Locate every malaria parasite.
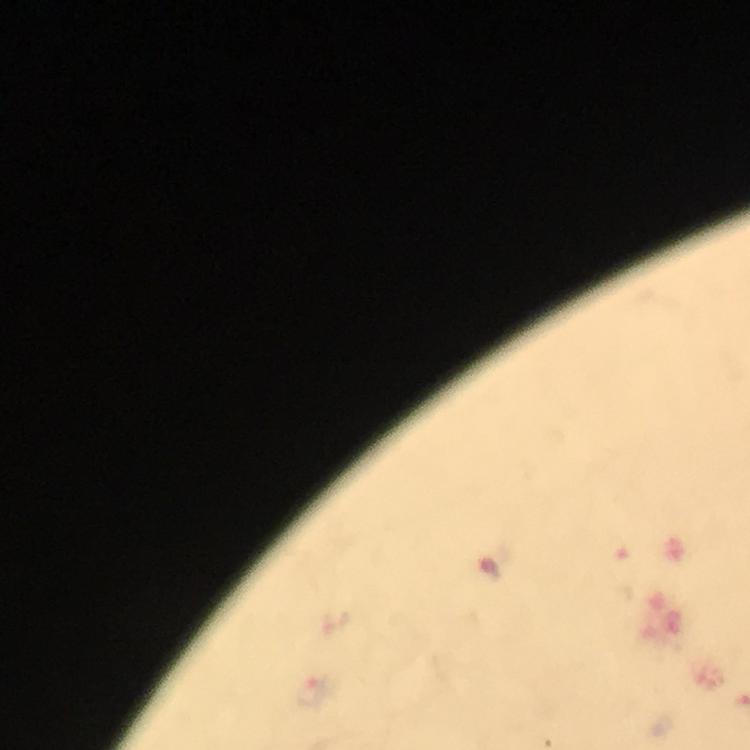

Approximate centers as {x, y} in pixels.
Malaria parasites: {312, 692}.

Summary:
  - Immersion oil: used
  - Capture: smartphone camera through the microscope
  - Image size: 750×750 pixels
  - Magnification: 100x
  - Context: from a malaria diagnostic workup
  - Cropped from: one field of view
  - Preparation: thick blood film
  - Stain: Giemsa